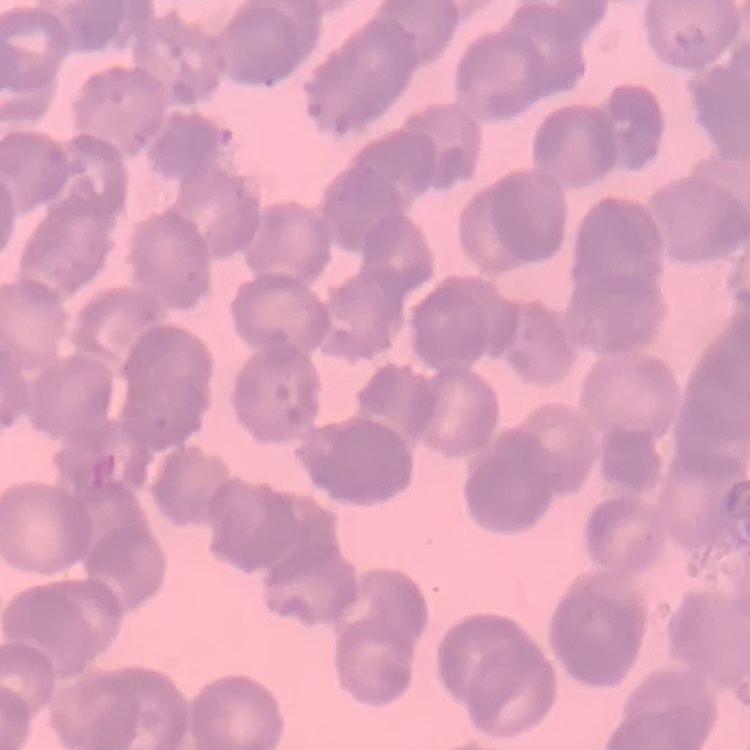

The red blood cells exhibit rouleaux formation. One tile cut from a larger photomicrograph. Field's or Giemsa stain. Thin blood film.